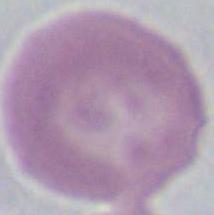
Summary:
  - Magnification: 1000x
  - Identification: erythrocyte
  - Modality: photomicrograph